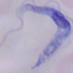 Captured at 1000x magnification. A trypanosome is shown. Photomicrograph.